Locate every Plasmodium parasite.
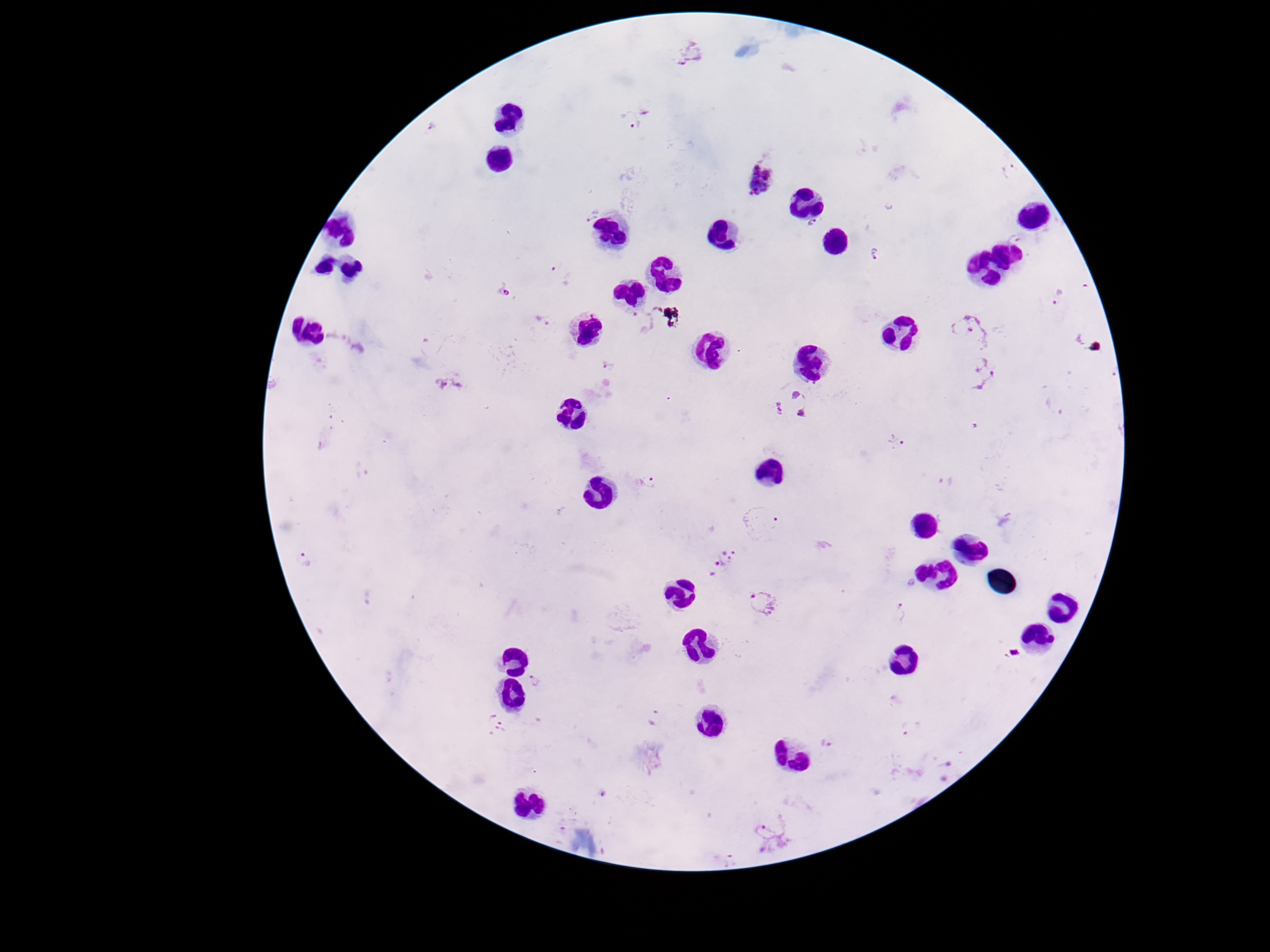

Approximate centers as (x, y) in pixels.
Plasmodium parasites: (691, 54), (646, 109), (627, 123), (429, 127), (761, 180), (589, 214), (813, 226), (1015, 238), (876, 254), (560, 278), (505, 290), (1058, 296), (542, 322), (642, 322), (971, 332), (353, 343), (606, 362), (978, 371), (449, 384), (792, 405), (1054, 406), (897, 443), (945, 480), (649, 484), (761, 525), (304, 560), (720, 563), (762, 604), (901, 614), (1012, 654), (535, 681), (654, 715), (495, 726), (912, 728), (828, 742), (940, 770), (774, 836), (732, 858).

100x magnification. Single field of view. Thick blood film. Image is 1270×952 pixels. Smartphone photograph taken through the microscope eyepiece. Giemsa-stained preparation. Patient malaria status: positive.